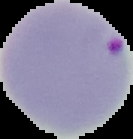
Result: malaria parasites identified. Image is 133×139 pixels. The area outside the segmented cell region is set to black. From a thin blood film.